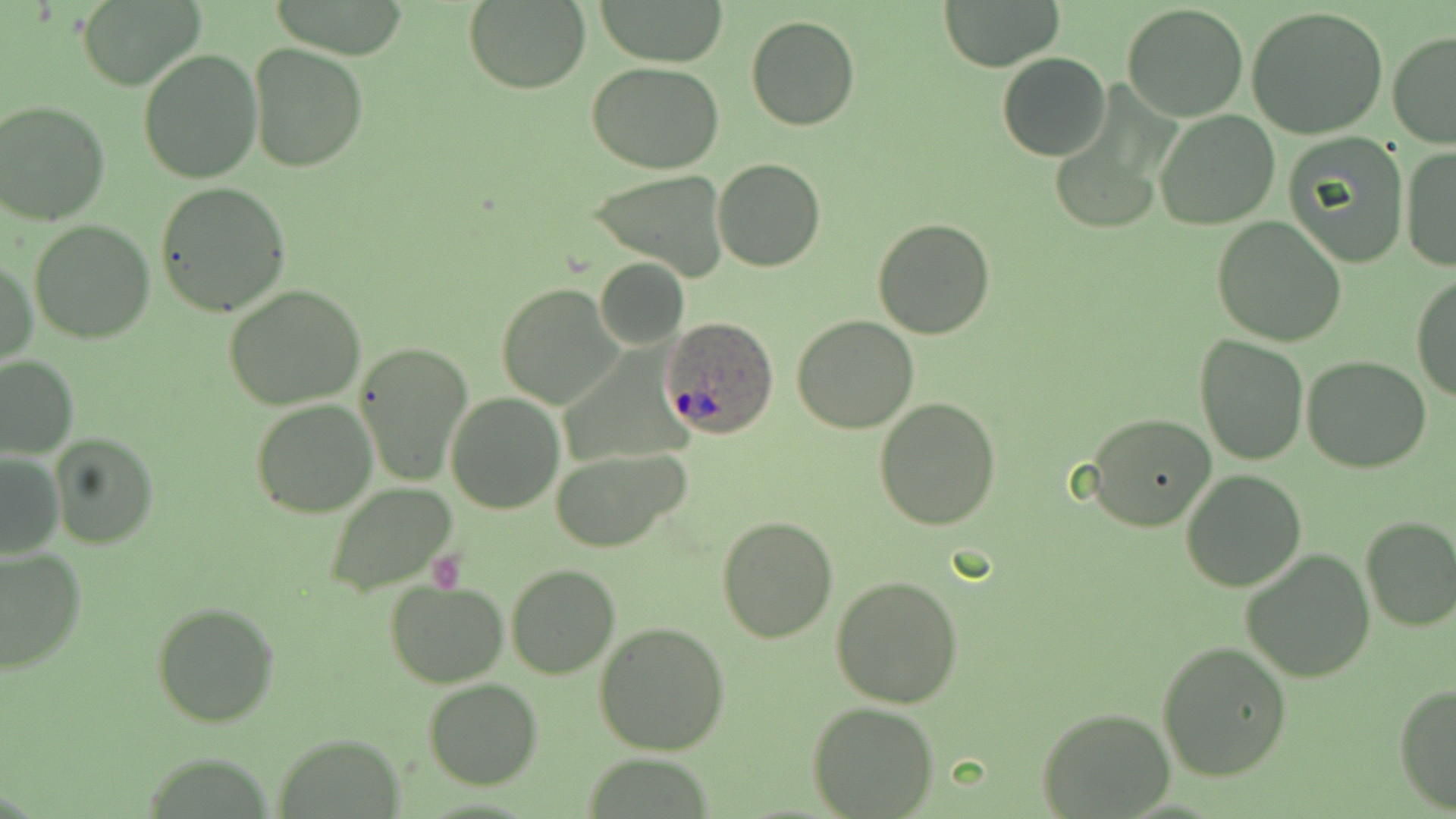
slide_level_diagnosis: Plasmodium ovale
magnification: 1000x
uninfected_red_blood_cell_locations: 'approximate bounding boxes as named x1/y1/x2/y2 corners in pixels: (x1=75, y1=0, x2=207, y2=91), (x1=598, y1=0, x2=728, y2=67), (x1=939, y1=0, x2=1065, y2=71), (x1=463, y1=1, x2=590, y2=92), (x1=1122, y1=5, x2=1246, y2=122), (x1=1248, y1=6, x2=1388, y2=139), (x1=747, y1=16, x2=860, y2=131), (x1=1387, y1=33, x2=1456, y2=150), (x1=247, y1=42, x2=369, y2=173), (x1=137, y1=49, x2=262, y2=185), (x1=997, y1=52, x2=1111, y2=160), (x1=588, y1=61, x2=723, y2=174), (x1=1, y1=98, x2=112, y2=225), (x1=1154, y1=109, x2=1280, y2=230), (x1=1282, y1=132, x2=1410, y2=269), (x1=1399, y1=145, x2=1456, y2=274), (x1=714, y1=159, x2=824, y2=272), (x1=590, y1=170, x2=729, y2=280), (x1=154, y1=182, x2=293, y2=317), (x1=872, y1=217, x2=995, y2=339), (x1=1212, y1=217, x2=1347, y2=347), (x1=28, y1=219, x2=155, y2=344), (x1=1, y1=256, x2=37, y2=367), (x1=594, y1=258, x2=689, y2=349), (x1=1412, y1=275, x2=1456, y2=404), (x1=495, y1=283, x2=623, y2=409), (x1=224, y1=285, x2=368, y2=410), (x1=791, y1=314, x2=919, y2=434), (x1=1194, y1=335, x2=1308, y2=466), (x1=354, y1=342, x2=473, y2=485), (x1=0, y1=355, x2=79, y2=458), (x1=1303, y1=356, x2=1432, y2=473), (x1=445, y1=391, x2=564, y2=514), (x1=875, y1=396, x2=1002, y2=530), (x1=249, y1=399, x2=379, y2=519), (x1=1085, y1=413, x2=1215, y2=532), (x1=49, y1=433, x2=158, y2=550), (x1=550, y1=445, x2=693, y2=553), (x1=0, y1=452, x2=64, y2=559), (x1=1181, y1=470, x2=1306, y2=591), (x1=326, y1=483, x2=457, y2=597), (x1=716, y1=515, x2=838, y2=643), (x1=1360, y1=516, x2=1456, y2=633), (x1=0, y1=547, x2=87, y2=679), (x1=1241, y1=548, x2=1375, y2=681), (x1=505, y1=564, x2=619, y2=679), (x1=831, y1=574, x2=963, y2=707), (x1=385, y1=580, x2=510, y2=688), (x1=150, y1=601, x2=279, y2=727), (x1=594, y1=622, x2=731, y2=755), (x1=1156, y1=641, x2=1293, y2=780), (x1=422, y1=678, x2=544, y2=789), (x1=1393, y1=681, x2=1456, y2=813), (x1=808, y1=700, x2=939, y2=817), (x1=1038, y1=707, x2=1173, y2=816), (x1=273, y1=733, x2=405, y2=818)'
preparation: thin blood film
image_size: 1456×819 pixels
modality: optical microscopy
field_of_view: one of a larger specimen
stain: May-Grünwald-Giemsa
plasmodium_ovale_infected_red_blood_cell_locations: 'approximate bounding boxes as named x1/y1/x2/y2 corners in pixels: (x1=660, y1=317, x2=780, y2=438)'